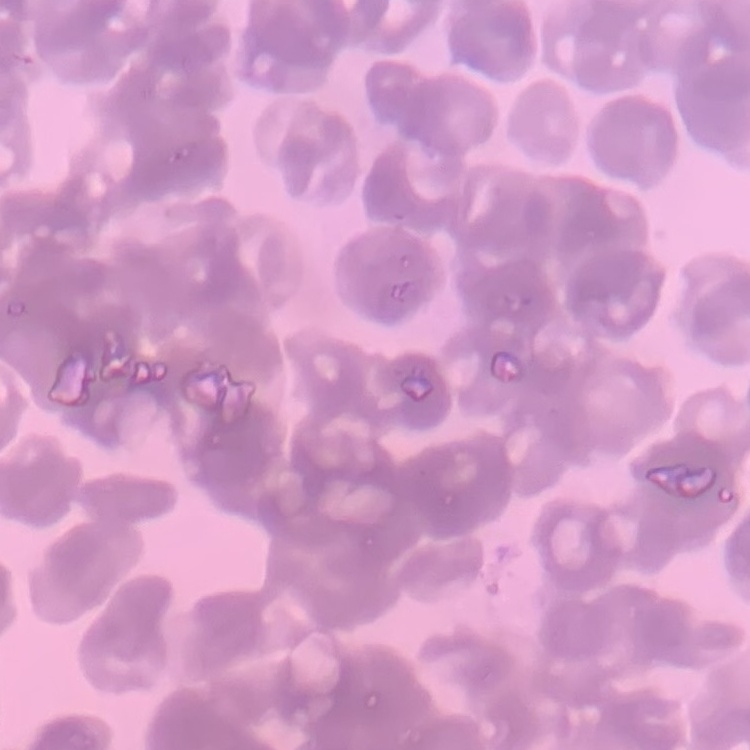 The red blood cells exhibit rouleaux formation. Stained with either Field's or Giemsa. Thin peripheral smear. One tile cut from a larger photomicrograph.